Classify this cell by malaria status.
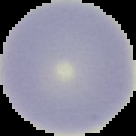

Uninfected.

Image is 136×136 pixels. From a thin blood smear. The area outside the segmented cell region is set to black.